Assess this cell for malaria.
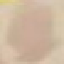

Uninfected.

Photographed with a smartphone camera at the microscope eyepiece. Giemsa-stained preparation. Cell patch, automatically extracted from a larger field of view and resized to 64 × 64 pixels. Thin blood smear.